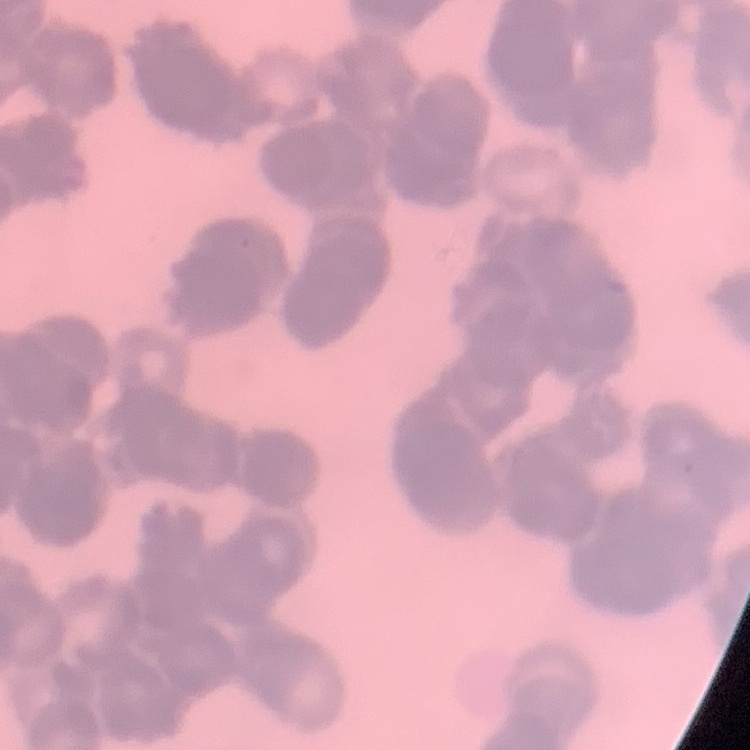
The erythrocytes exhibit rouleaux formation. Thin blood smear. Square crop of a larger photomicrograph. Stained with either Field's or Giemsa.